Identify the parasite.
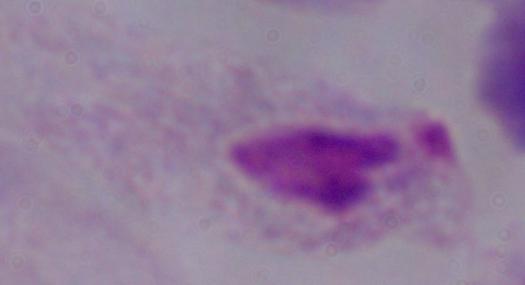
A trichomonad.

Summary:
  - Modality: photomicrograph
  - Magnification: 1000x